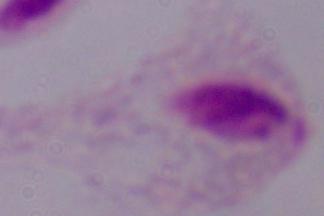
Captured at 1000x magnification. A trichomonad is seen. Photomicrograph.